Locate malaria parasites and leukocytes.
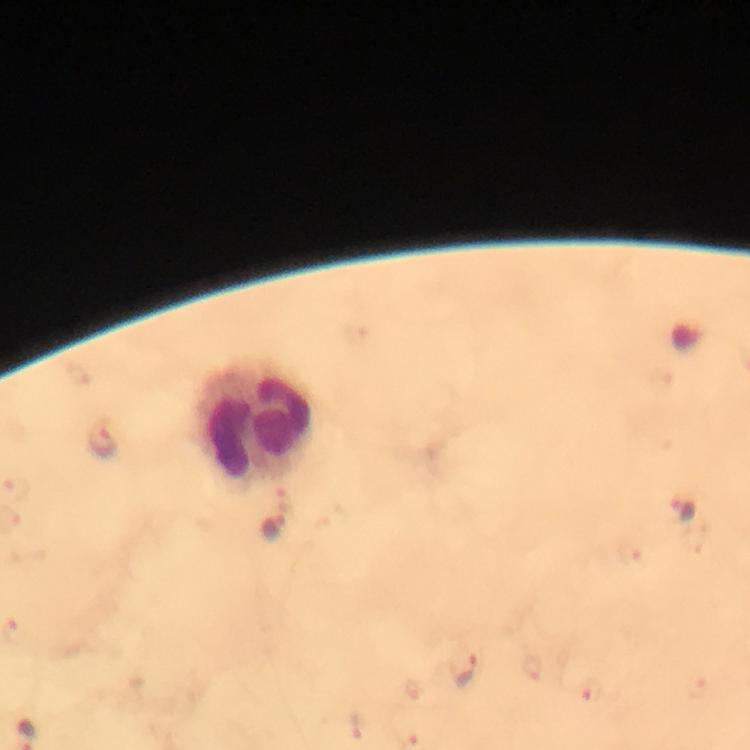

Approximate centers as {x, y} in pixels.
Malaria parasites: {103, 445}, {685, 511}, {273, 528}, {466, 673}.
Leukocytes: {254, 422}.

preparation: thick blood smear
immersion_oil: used
image_size: 750×750 pixels
context: from a diagnostic examination for malaria
cropped_from: a single field of view
stain: Giemsa
capture: smartphone camera through the microscope
magnification: 100x